State which parasite is depicted.
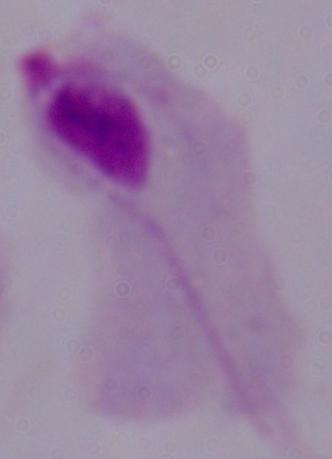
A trichomonad.

Summary:
  - Magnification: 1000x
  - Modality: photomicrograph